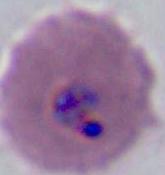

{
  "identification": "Plasmodium",
  "magnification": "400x or 1000x",
  "modality": "photomicrograph"
}